Identify the preparation type.
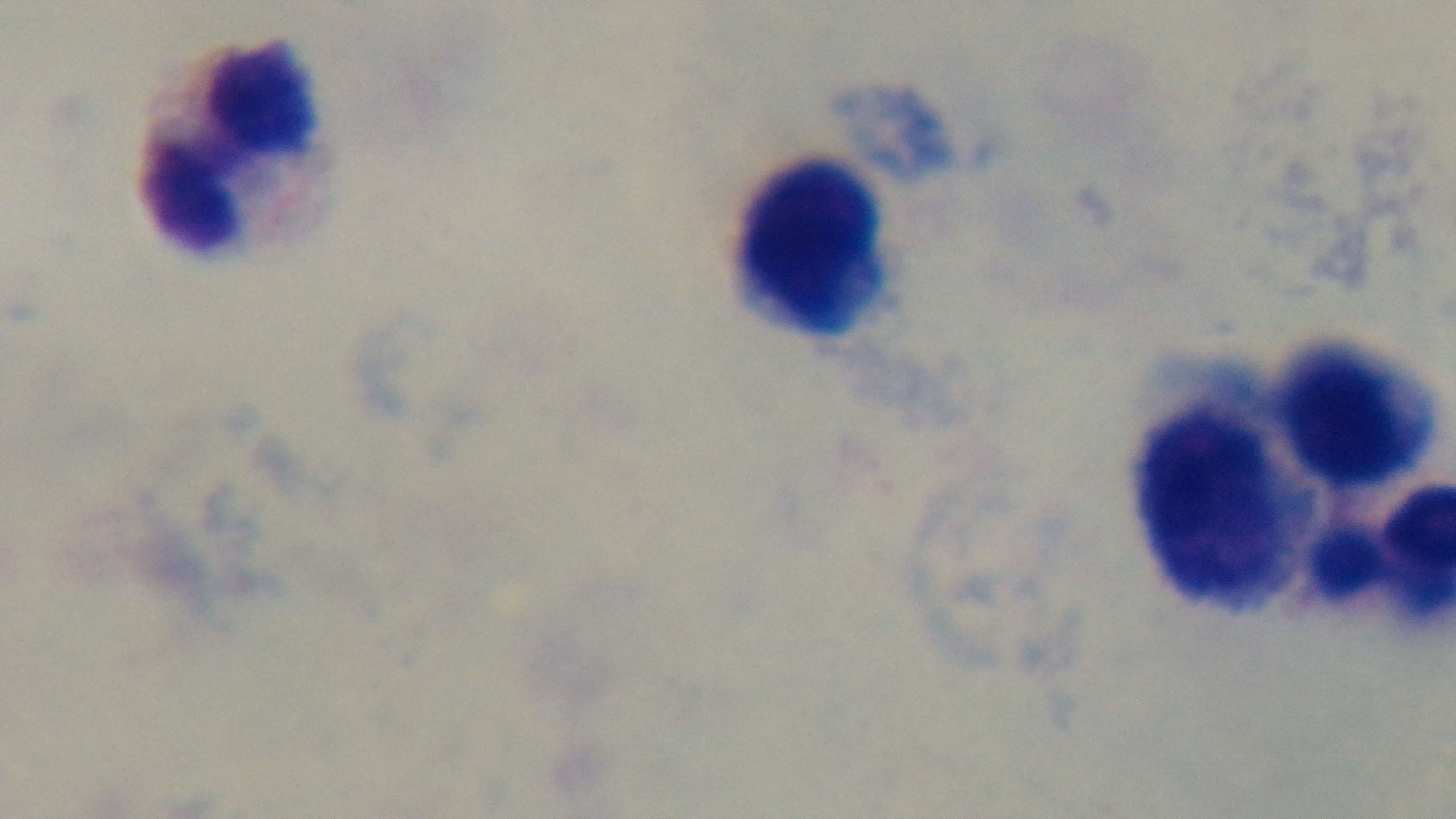

It is a thick blood film.

100x oil-immersion objective. Photomicrograph. Giemsa-stained. One field from the slide. Mounted 4K digital camera. Malaria status: negative.